Assess this cell for malaria.
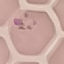
Uninfected.

preparation: thin blood smear
image_type: automatically extracted cell patch, resized to 64 × 64 pixels
capture: smartphone through the microscope eyepiece
stain: Giemsa